Report the malaria status of this cell.
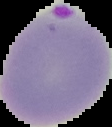
It is parasitized.

image_size: 112×127 pixels
image_type: cell region segmented out of the field of view; surrounding area masked to black
preparation: thin blood smear